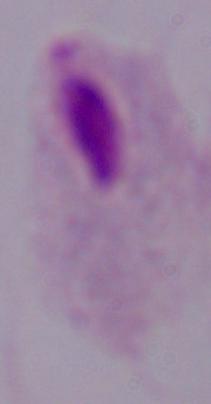
identification = trichomonad
magnification = 1000x
modality = photomicrograph